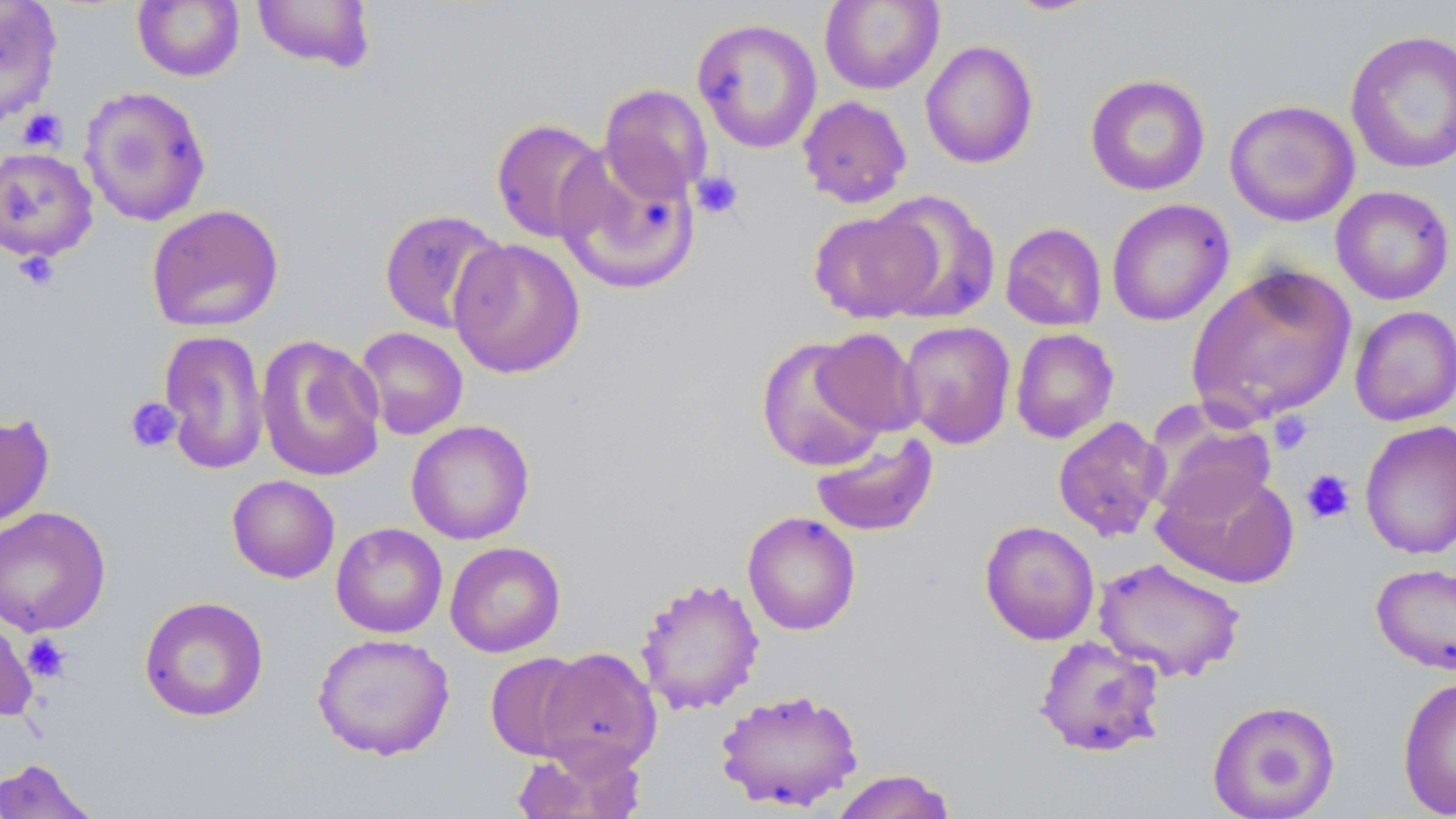
Approximate bounding boxes as (x1, y1, x2, y2) in pixels. Platelet locations: (17, 108, 67, 152), (691, 171, 744, 219), (14, 250, 59, 290), (124, 397, 182, 453), (1269, 412, 1312, 454), (1301, 469, 1356, 524), (21, 632, 71, 683). Uninfected red blood cell locations: (0, 0, 63, 126), (132, 0, 245, 82), (251, 0, 376, 72), (1003, 0, 1102, 16), (819, 1, 944, 94), (691, 17, 822, 154), (1345, 28, 1456, 174), (920, 40, 1038, 169), (1084, 74, 1211, 197), (599, 83, 713, 203), (79, 86, 212, 227), (797, 95, 912, 208), (1224, 99, 1360, 226), (491, 118, 610, 243), (555, 143, 700, 294), (0, 146, 98, 262), (1331, 185, 1455, 305), (870, 190, 1001, 324), (1106, 199, 1234, 326), (146, 204, 284, 332), (378, 208, 507, 334), (808, 210, 939, 323), (1000, 222, 1107, 331), (448, 238, 585, 379), (1185, 262, 1357, 425), (1350, 305, 1455, 426), (898, 320, 1016, 450), (354, 326, 469, 440), (813, 327, 922, 438), (1010, 328, 1119, 444), (157, 329, 269, 475), (256, 334, 386, 482), (755, 336, 888, 474), (1146, 410, 1277, 524), (0, 413, 55, 528), (1052, 415, 1170, 542), (406, 419, 534, 545), (1360, 421, 1456, 560), (810, 432, 939, 537), (1153, 467, 1300, 588), (227, 474, 340, 583), (0, 506, 111, 637), (743, 511, 861, 635), (979, 520, 1100, 646), (331, 523, 448, 638), (445, 541, 565, 657), (1092, 557, 1246, 682), (1370, 563, 1456, 676), (635, 576, 765, 716), (139, 595, 269, 722), (0, 616, 37, 721), (311, 632, 456, 761), (1033, 635, 1166, 758), (535, 647, 662, 774), (484, 652, 590, 761), (1397, 676, 1456, 817), (714, 688, 864, 812), (1207, 699, 1340, 819), (509, 744, 646, 819), (0, 758, 99, 818), (829, 768, 958, 819). Slide-level diagnosis: no evidence of blood parasites. Optical microscopy. May-Grünwald-Giemsa stain. Thin blood film. One field of a larger specimen. Captured at 1000x magnification. Image is 1456×819 pixels.